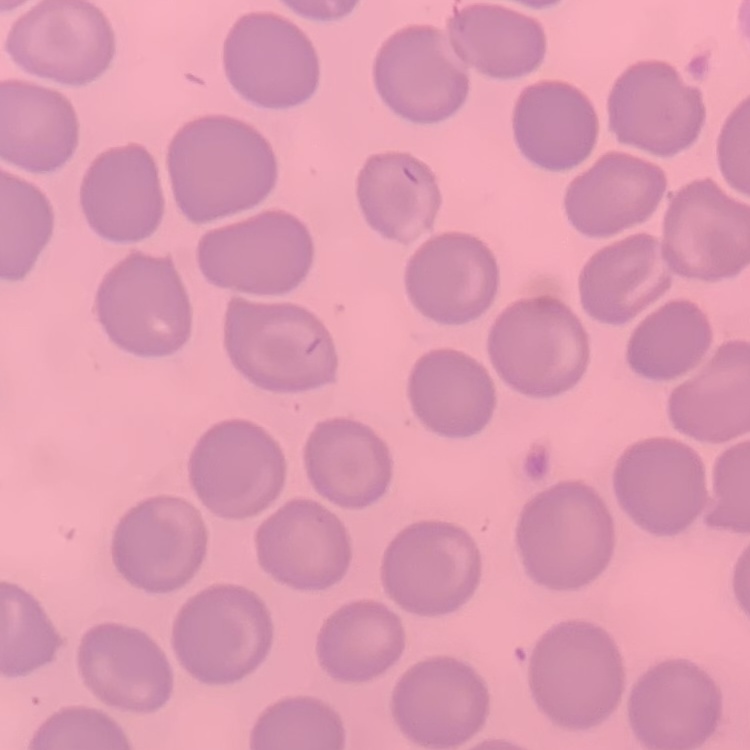

erythrocyte morphology = no rouleaux formation
preparation = thin blood smear
stain = Field's or Giemsa
image type = square crop of a larger photomicrograph